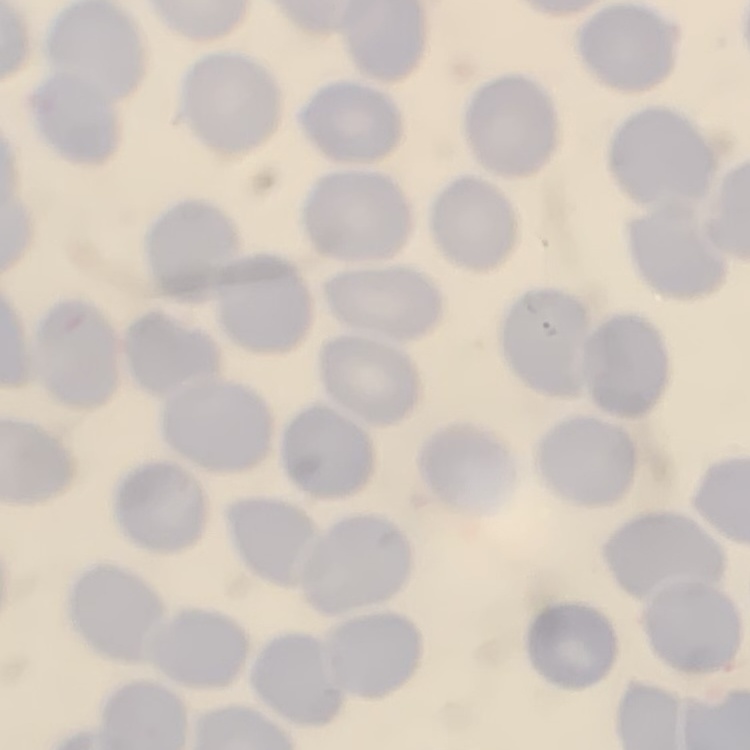

Summary:
  - Red blood cell morphology: no rouleaux formation
  - Image type: one tile cut from a larger photomicrograph
  - Stain: Field's or Giemsa
  - Preparation: thin peripheral smear